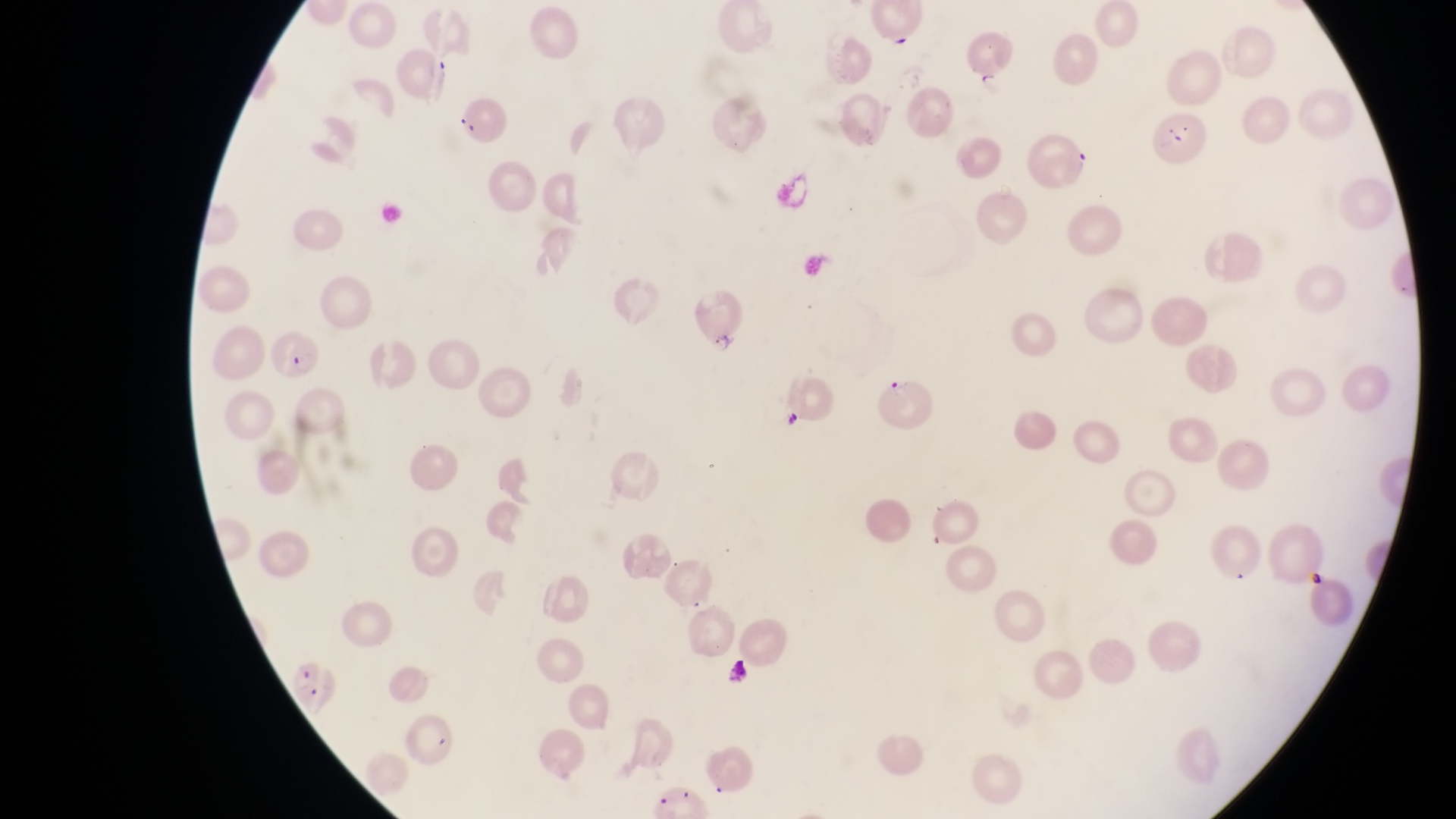
capture = smartphone photograph through the eyepiece of an Olympus CX-23 microscope
artifact (platelet-like body, stain precipitate, or debris) locations = approximate bounding boxes as [left, top, right, bottom] in pixels: [782, 407, 809, 439]
magnification = 1000x
parasitised red blood cell locations = approximate bounding boxes as [left, top, right, bottom] in pixels: [394, 45, 454, 101], [1033, 125, 1093, 196], [690, 288, 749, 354], [267, 323, 328, 383], [877, 368, 935, 427]
image size = 1456×819 pixels
country = Uganda
preparation = thin blood smear
field of view = single